Give the position of every leukocyte visible.
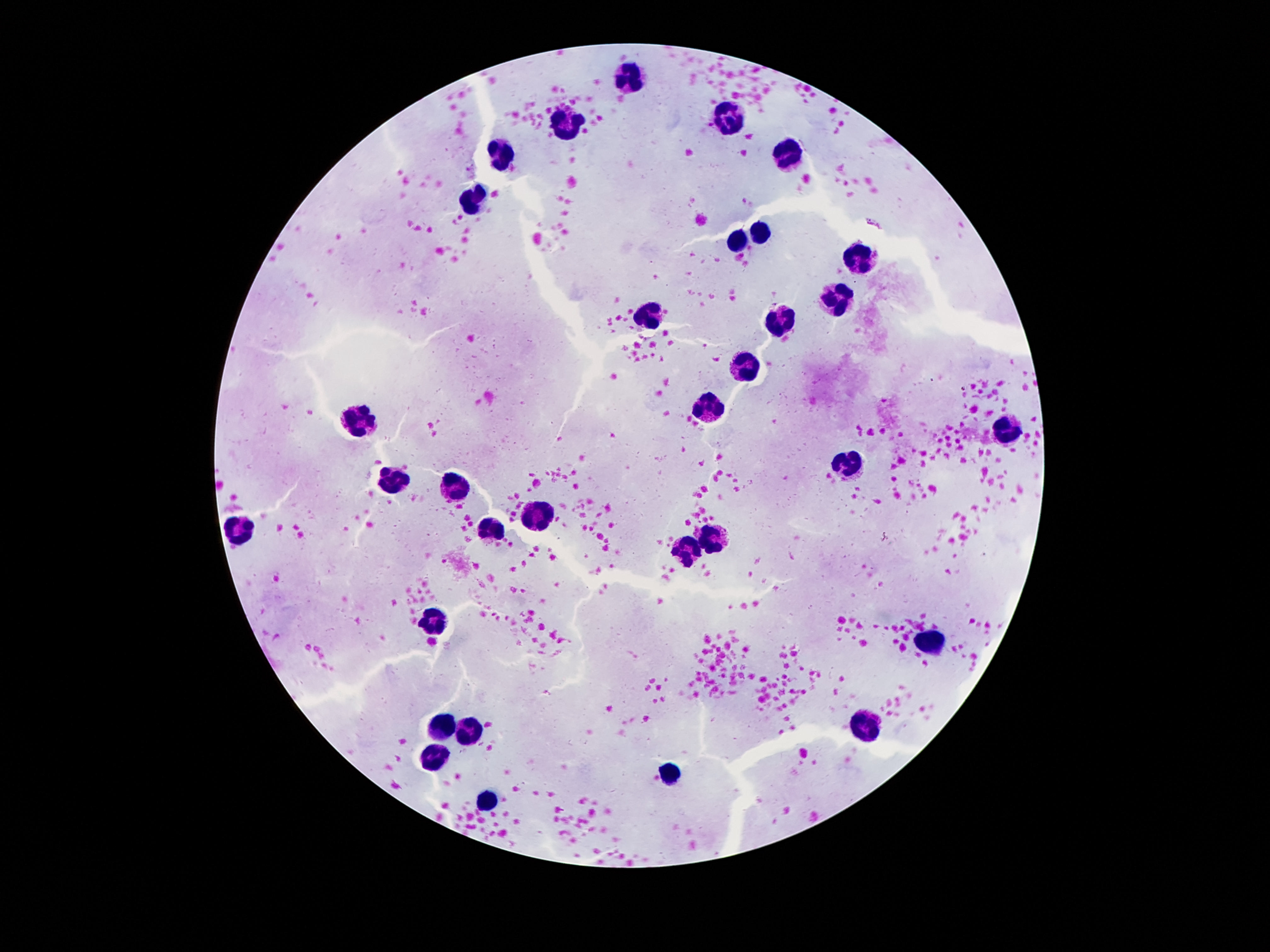

Approximate centers as {x, y} in pixels.
Leukocytes: {630, 78}, {728, 118}, {565, 125}, {498, 153}, {789, 155}, {470, 201}, {763, 232}, {738, 240}, {864, 251}, {836, 299}, {646, 316}, {777, 323}, {744, 363}, {715, 402}, {362, 421}, {1006, 428}, {850, 461}, {390, 479}, {455, 489}, {540, 509}, {239, 529}, {495, 529}, {714, 540}, {684, 552}, {434, 618}, {929, 643}, {868, 723}, {444, 730}, {472, 730}, {437, 758}, {670, 771}, {488, 800}.

Summary:
  - Preparation: thick blood film
  - Stain: Giemsa
  - Field of view: one from this slide
  - Image size: 1270×952 pixels
  - Patient malaria status: negative
  - Capture: smartphone camera through the microscope eyepiece
  - Magnification: 100x